Locate every Plasmodium malariae-infected red blood cell.
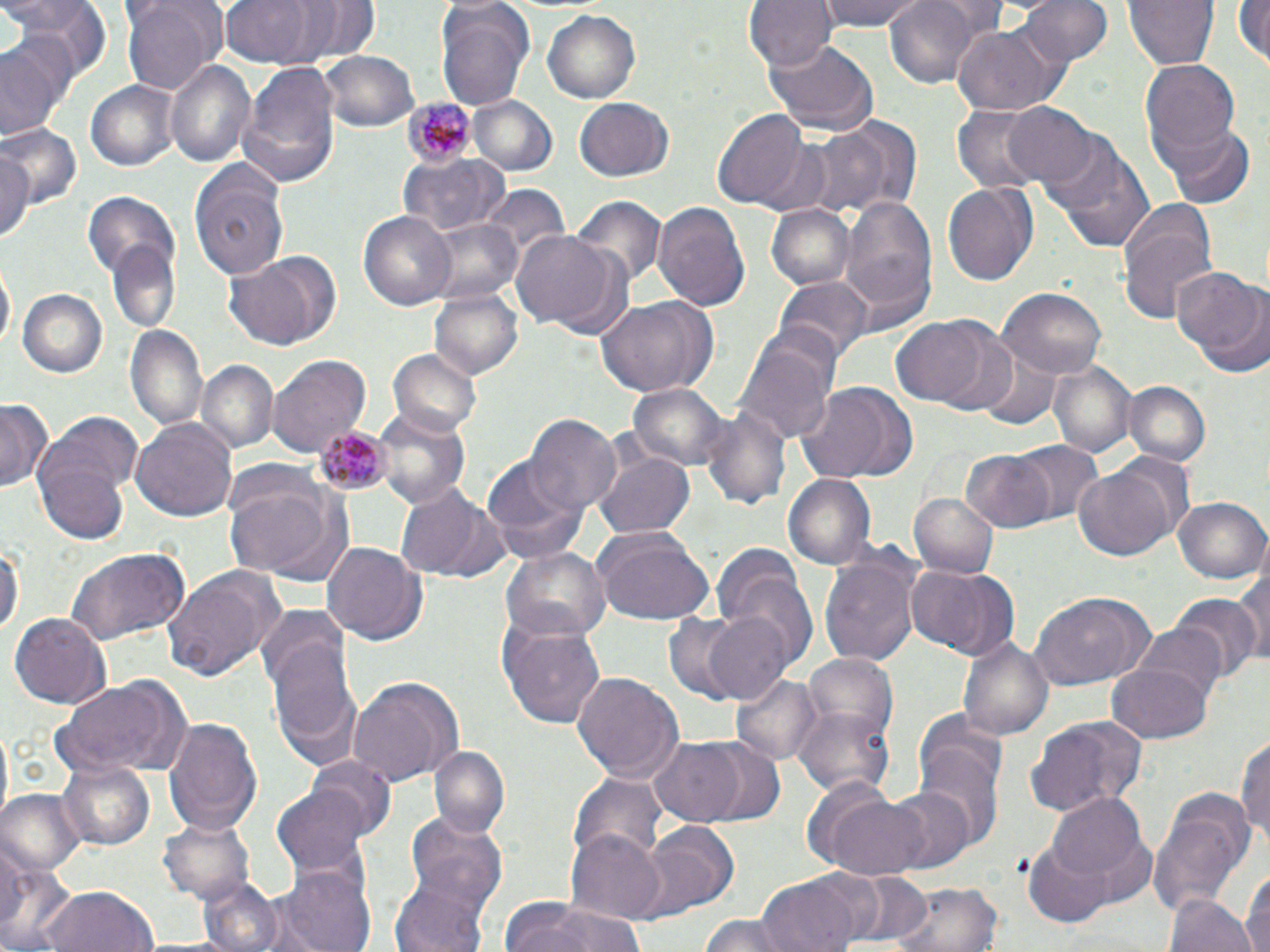
Approximate bounding boxes as named x1/y1/x2/y2 corners in pixels.
Plasmodium malariae-infected red blood cells: (x1=400, y1=95, x2=472, y2=166), (x1=315, y1=425, x2=387, y2=493).

Uninfected red blood cell locations: (x1=4, y1=0, x2=109, y2=83), (x1=119, y1=0, x2=225, y2=95), (x1=219, y1=0, x2=312, y2=69), (x1=743, y1=0, x2=835, y2=73), (x1=817, y1=0, x2=924, y2=31), (x1=884, y1=0, x2=990, y2=89), (x1=1016, y1=0, x2=1113, y2=69), (x1=1123, y1=0, x2=1218, y2=71), (x1=1233, y1=0, x2=1270, y2=70), (x1=290, y1=1, x2=382, y2=64), (x1=437, y1=5, x2=534, y2=112), (x1=544, y1=10, x2=641, y2=102), (x1=950, y1=22, x2=1070, y2=114), (x1=2, y1=35, x2=72, y2=139), (x1=762, y1=37, x2=879, y2=136), (x1=319, y1=50, x2=417, y2=131), (x1=241, y1=59, x2=339, y2=179), (x1=1140, y1=60, x2=1239, y2=155), (x1=167, y1=61, x2=255, y2=168), (x1=85, y1=80, x2=180, y2=171), (x1=469, y1=96, x2=559, y2=178), (x1=575, y1=98, x2=674, y2=182), (x1=1005, y1=103, x2=1099, y2=189), (x1=952, y1=104, x2=1048, y2=193), (x1=712, y1=107, x2=816, y2=212), (x1=812, y1=119, x2=913, y2=220), (x1=1159, y1=123, x2=1255, y2=207), (x1=2, y1=126, x2=80, y2=213), (x1=1052, y1=140, x2=1156, y2=254), (x1=0, y1=150, x2=36, y2=249), (x1=399, y1=154, x2=507, y2=237), (x1=190, y1=163, x2=290, y2=279), (x1=943, y1=179, x2=1039, y2=289), (x1=481, y1=185, x2=571, y2=272), (x1=82, y1=191, x2=181, y2=278), (x1=837, y1=194, x2=937, y2=326), (x1=569, y1=197, x2=664, y2=290), (x1=652, y1=200, x2=752, y2=312), (x1=768, y1=203, x2=856, y2=291), (x1=1117, y1=204, x2=1217, y2=321), (x1=357, y1=210, x2=457, y2=311), (x1=421, y1=218, x2=526, y2=305), (x1=510, y1=230, x2=617, y2=331), (x1=105, y1=244, x2=180, y2=333), (x1=222, y1=253, x2=338, y2=350), (x1=1, y1=263, x2=14, y2=357), (x1=1171, y1=270, x2=1270, y2=375), (x1=774, y1=275, x2=873, y2=365), (x1=18, y1=289, x2=107, y2=378), (x1=999, y1=289, x2=1106, y2=379), (x1=432, y1=290, x2=521, y2=377), (x1=595, y1=296, x2=718, y2=396), (x1=892, y1=317, x2=993, y2=408), (x1=125, y1=324, x2=209, y2=435), (x1=928, y1=324, x2=1023, y2=418), (x1=738, y1=339, x2=836, y2=445), (x1=390, y1=350, x2=482, y2=437), (x1=977, y1=350, x2=1065, y2=431), (x1=266, y1=354, x2=371, y2=461), (x1=1049, y1=361, x2=1136, y2=458), (x1=198, y1=363, x2=276, y2=452), (x1=627, y1=382, x2=728, y2=473), (x1=1123, y1=382, x2=1212, y2=468), (x1=795, y1=383, x2=915, y2=484), (x1=1, y1=397, x2=54, y2=494), (x1=702, y1=405, x2=792, y2=509), (x1=370, y1=407, x2=474, y2=509), (x1=528, y1=414, x2=619, y2=512), (x1=130, y1=417, x2=239, y2=525), (x1=34, y1=421, x2=141, y2=542), (x1=1012, y1=441, x2=1104, y2=526), (x1=594, y1=446, x2=695, y2=538), (x1=961, y1=449, x2=1055, y2=531), (x1=481, y1=454, x2=589, y2=563), (x1=1074, y1=467, x2=1175, y2=561), (x1=224, y1=469, x2=352, y2=585), (x1=783, y1=473, x2=877, y2=571), (x1=394, y1=485, x2=497, y2=580), (x1=909, y1=491, x2=998, y2=578), (x1=1175, y1=495, x2=1268, y2=584), (x1=592, y1=531, x2=715, y2=625), (x1=0, y1=537, x2=21, y2=641), (x1=322, y1=541, x2=428, y2=645), (x1=500, y1=546, x2=608, y2=642), (x1=62, y1=547, x2=190, y2=647), (x1=820, y1=556, x2=918, y2=668), (x1=715, y1=559, x2=820, y2=671), (x1=909, y1=565, x2=1007, y2=657), (x1=163, y1=567, x2=280, y2=682), (x1=1234, y1=567, x2=1269, y2=670), (x1=1029, y1=593, x2=1147, y2=689), (x1=1174, y1=595, x2=1259, y2=683), (x1=257, y1=605, x2=353, y2=692), (x1=701, y1=611, x2=795, y2=704), (x1=9, y1=612, x2=108, y2=709), (x1=661, y1=612, x2=753, y2=704), (x1=500, y1=619, x2=605, y2=730), (x1=1135, y1=622, x2=1229, y2=706), (x1=269, y1=630, x2=363, y2=769), (x1=959, y1=634, x2=1054, y2=741), (x1=803, y1=653, x2=897, y2=737), (x1=1107, y1=662, x2=1213, y2=742), (x1=732, y1=670, x2=824, y2=767), (x1=573, y1=673, x2=681, y2=785), (x1=52, y1=677, x2=191, y2=779), (x1=349, y1=678, x2=462, y2=785), (x1=796, y1=705, x2=896, y2=798), (x1=162, y1=714, x2=262, y2=837), (x1=914, y1=714, x2=1008, y2=842), (x1=1024, y1=714, x2=1147, y2=816), (x1=1235, y1=730, x2=1269, y2=849), (x1=649, y1=738, x2=746, y2=824), (x1=694, y1=740, x2=786, y2=826), (x1=429, y1=744, x2=511, y2=839), (x1=304, y1=755, x2=397, y2=839), (x1=57, y1=761, x2=155, y2=851), (x1=573, y1=772, x2=667, y2=869), (x1=275, y1=784, x2=372, y2=875), (x1=882, y1=785, x2=974, y2=874), (x1=1149, y1=788, x2=1258, y2=918), (x1=0, y1=790, x2=84, y2=878), (x1=821, y1=792, x2=936, y2=881), (x1=1050, y1=792, x2=1150, y2=884), (x1=404, y1=811, x2=508, y2=912), (x1=160, y1=816, x2=257, y2=905), (x1=636, y1=820, x2=739, y2=921), (x1=565, y1=829, x2=666, y2=922), (x1=0, y1=842, x2=77, y2=952), (x1=1026, y1=843, x2=1112, y2=927), (x1=281, y1=863, x2=376, y2=952), (x1=1240, y1=866, x2=1269, y2=952), (x1=834, y1=868, x2=935, y2=948), (x1=389, y1=874, x2=493, y2=952), (x1=195, y1=878, x2=288, y2=952), (x1=756, y1=879, x2=856, y2=952), (x1=888, y1=880, x2=1001, y2=952), (x1=41, y1=885, x2=159, y2=952), (x1=1168, y1=894, x2=1256, y2=952), (x1=502, y1=898, x2=645, y2=952), (x1=701, y1=912, x2=797, y2=952). Slide-level diagnosis: Plasmodium malariae. Image is 1270×952 pixels. 1000x magnification. Thin blood film. May-Grünwald-Giemsa-stained preparation. Light microscopy. One field of a larger specimen.